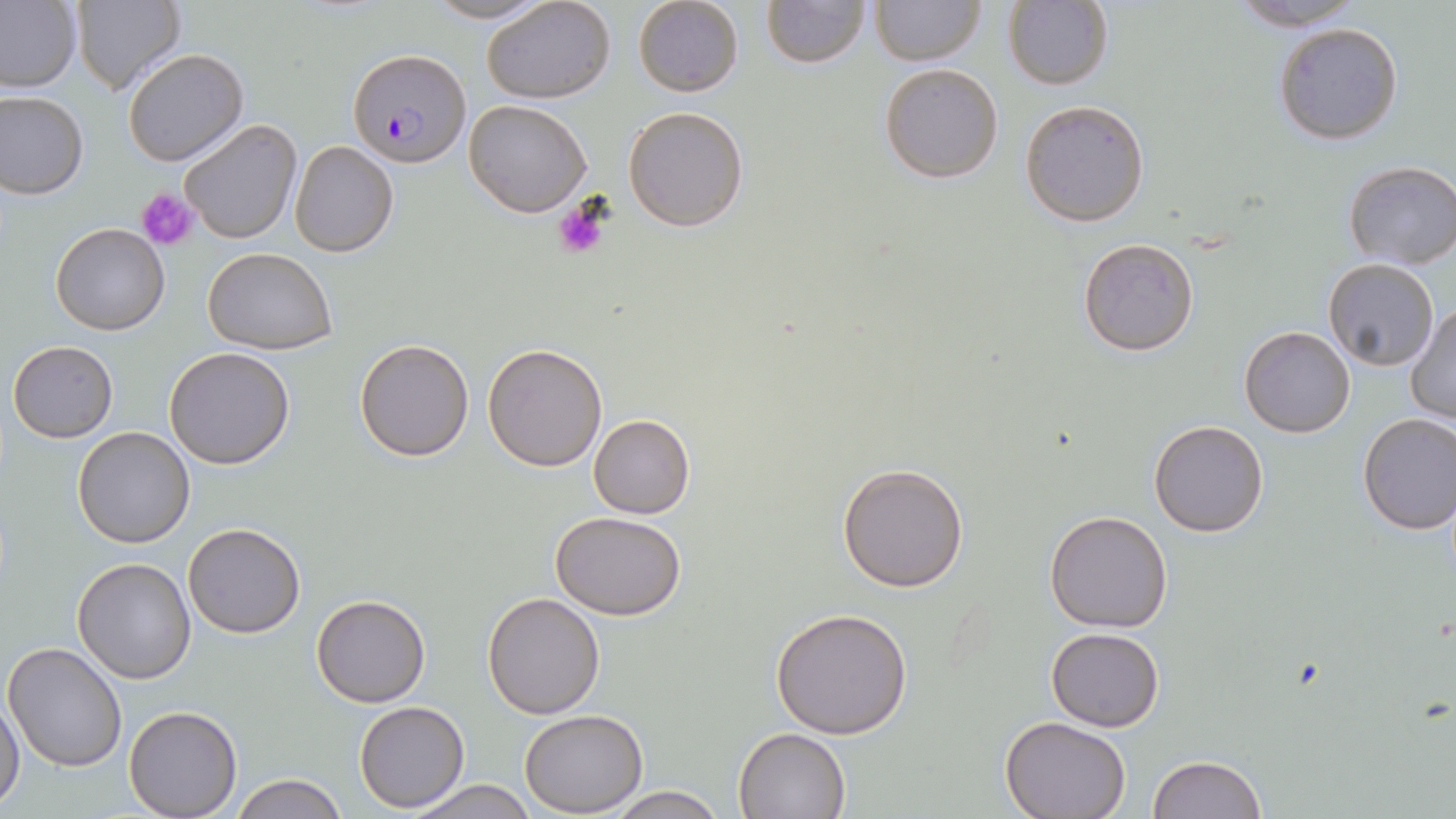

Approximate bounding boxes as [x1, y1, x2, y2] in pixels. Uninfected red blood cell locations: [0, 0, 83, 93], [71, 0, 186, 94], [422, 0, 553, 24], [482, 0, 617, 104], [633, 0, 744, 98], [760, 0, 871, 68], [871, 0, 984, 66], [1005, 1, 1115, 92], [1222, 2, 1369, 30], [1273, 22, 1404, 146], [123, 47, 248, 167], [879, 63, 1004, 184], [0, 90, 88, 199], [463, 99, 592, 217], [1019, 99, 1152, 228], [623, 104, 750, 231], [177, 116, 303, 244], [288, 139, 401, 257], [1342, 161, 1455, 269], [50, 222, 170, 335], [1077, 236, 1200, 356], [201, 247, 337, 353], [1321, 259, 1439, 371], [1407, 301, 1456, 427], [1238, 326, 1356, 438], [353, 338, 474, 461], [6, 339, 118, 443], [482, 343, 609, 471], [1188, 344, 1317, 486], [163, 346, 295, 469], [1356, 412, 1456, 533], [588, 414, 695, 519], [1149, 419, 1270, 537], [73, 427, 196, 549], [836, 461, 970, 592], [1044, 508, 1174, 631], [549, 510, 691, 620], [183, 522, 306, 639], [73, 557, 198, 684], [481, 591, 605, 719], [311, 595, 430, 707], [769, 606, 915, 739], [1045, 627, 1165, 730], [4, 642, 128, 771], [1, 695, 25, 813], [354, 700, 469, 811], [123, 706, 243, 818], [519, 709, 648, 814], [999, 716, 1132, 819], [733, 726, 851, 818], [1148, 754, 1267, 818], [229, 773, 347, 819], [404, 779, 537, 819], [602, 789, 729, 819]. Platelet locations: [136, 188, 198, 251], [551, 200, 609, 262]. Plasmodium falciparum-infected red blood cell locations: [348, 48, 470, 167]. Slide-level diagnosis: Plasmodium falciparum. Optical microscopy. Image is 1456×819 pixels. Captured at 1000x magnification. One field of a larger specimen. Thin blood film. May-Grünwald-Giemsa-stained preparation.